Classify this cell by malaria status.
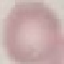
Uninfected.

preparation = thin blood smear
capture = smartphone through the microscope eyepiece
image type = cell patch, automatically extracted from a larger field of view and resized to 64 × 64 pixels
stain = Giemsa